Assess the morphology of the red blood cells.
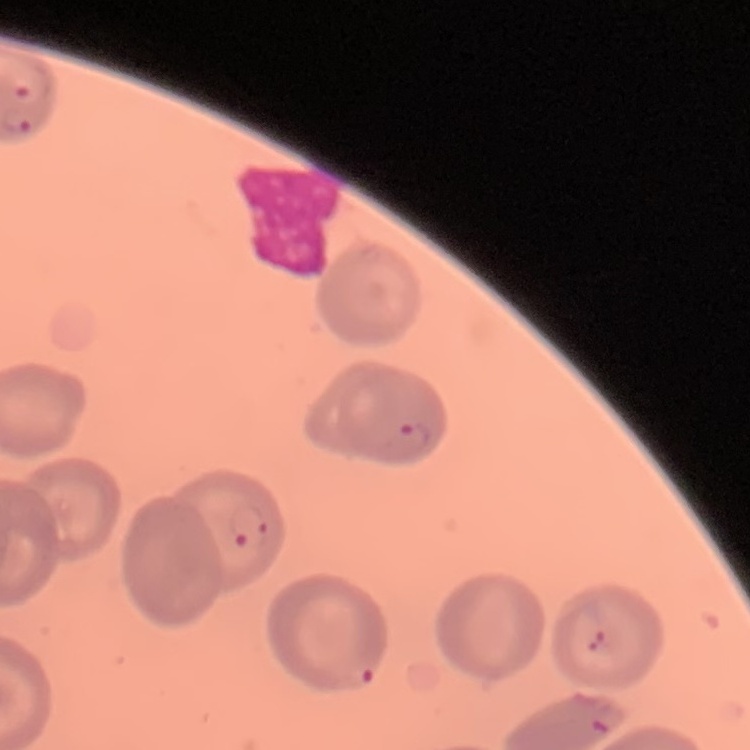

No rouleaux formation.

Summary:
  - Preparation: thin blood film
  - Image type: square crop of a larger photomicrograph
  - Stain: Field's or Giemsa